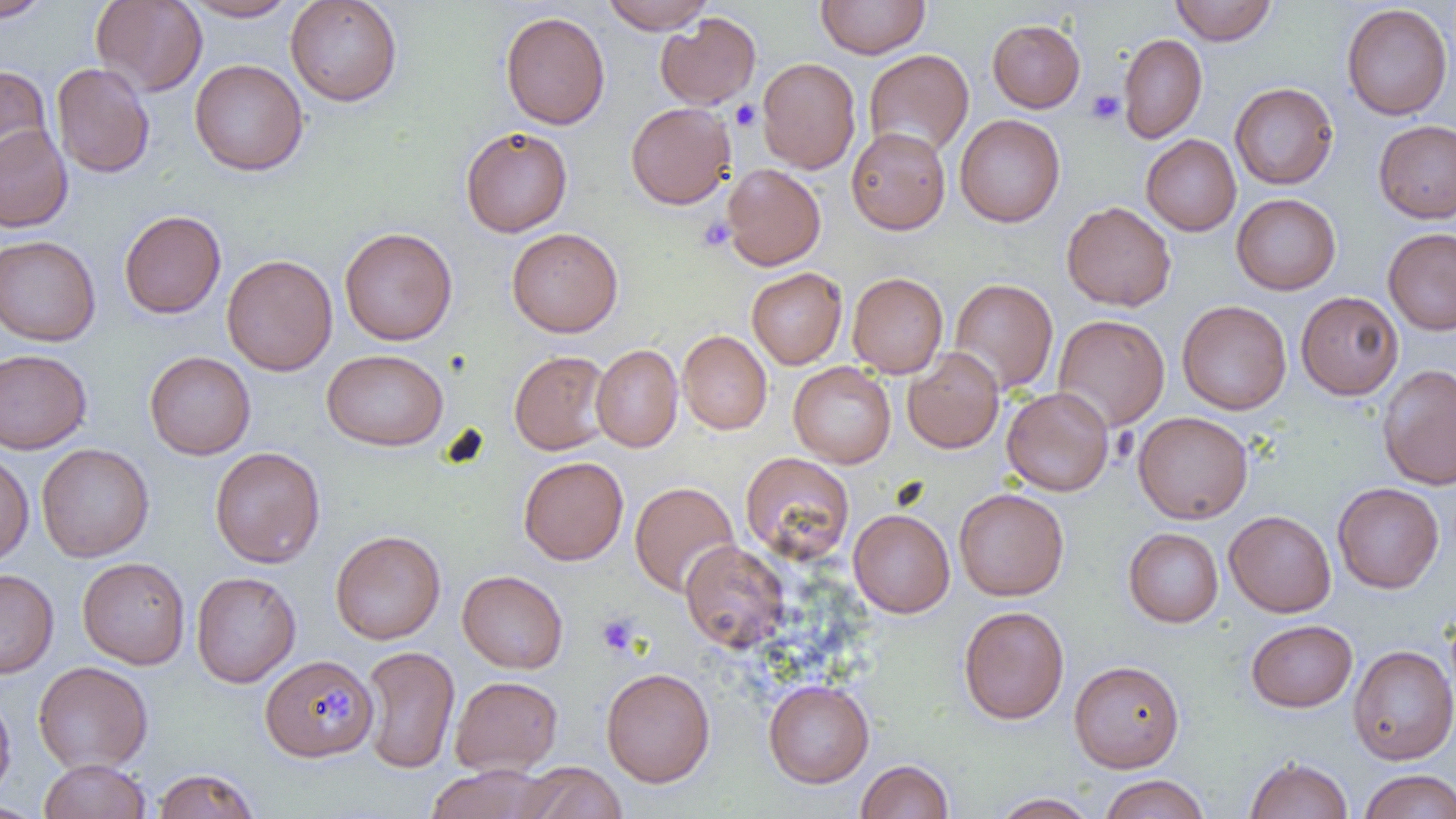 Approximate bounding boxes as named x1/y1/x2/y2 corners in pixels. Uninfected red blood cell locations: (x1=0, y1=0, x2=54, y2=22), (x1=182, y1=0, x2=302, y2=22), (x1=285, y1=0, x2=403, y2=106), (x1=599, y1=0, x2=716, y2=32), (x1=816, y1=0, x2=929, y2=59), (x1=1170, y1=0, x2=1276, y2=45), (x1=91, y1=1, x2=207, y2=96), (x1=1341, y1=3, x2=1453, y2=120), (x1=500, y1=11, x2=610, y2=130), (x1=655, y1=12, x2=761, y2=109), (x1=987, y1=19, x2=1085, y2=112), (x1=1118, y1=33, x2=1207, y2=143), (x1=863, y1=49, x2=974, y2=158), (x1=757, y1=57, x2=861, y2=174), (x1=189, y1=58, x2=309, y2=176), (x1=51, y1=63, x2=155, y2=178), (x1=0, y1=64, x2=54, y2=178), (x1=1229, y1=82, x2=1338, y2=189), (x1=626, y1=102, x2=736, y2=209), (x1=954, y1=114, x2=1065, y2=227), (x1=1373, y1=120, x2=1456, y2=223), (x1=0, y1=125, x2=73, y2=232), (x1=460, y1=126, x2=573, y2=237), (x1=846, y1=127, x2=951, y2=234), (x1=1141, y1=134, x2=1241, y2=236), (x1=722, y1=163, x2=826, y2=270), (x1=1231, y1=193, x2=1341, y2=294), (x1=1061, y1=201, x2=1176, y2=311), (x1=119, y1=210, x2=226, y2=319), (x1=339, y1=227, x2=457, y2=345), (x1=507, y1=227, x2=623, y2=337), (x1=1383, y1=227, x2=1456, y2=334), (x1=0, y1=235, x2=101, y2=346), (x1=222, y1=254, x2=338, y2=376), (x1=747, y1=268, x2=847, y2=369), (x1=847, y1=272, x2=948, y2=378), (x1=949, y1=278, x2=1058, y2=394), (x1=1296, y1=291, x2=1404, y2=399), (x1=1177, y1=300, x2=1292, y2=415), (x1=1053, y1=314, x2=1170, y2=431), (x1=678, y1=330, x2=772, y2=434), (x1=591, y1=344, x2=683, y2=452), (x1=0, y1=348, x2=92, y2=454), (x1=903, y1=348, x2=1004, y2=453), (x1=322, y1=349, x2=448, y2=451), (x1=509, y1=350, x2=612, y2=455), (x1=144, y1=351, x2=256, y2=459), (x1=788, y1=361, x2=896, y2=468), (x1=1377, y1=364, x2=1456, y2=489), (x1=1001, y1=386, x2=1114, y2=496), (x1=1133, y1=411, x2=1253, y2=523), (x1=36, y1=443, x2=154, y2=562), (x1=210, y1=446, x2=325, y2=568), (x1=0, y1=450, x2=34, y2=566), (x1=740, y1=452, x2=855, y2=564), (x1=518, y1=456, x2=628, y2=565), (x1=629, y1=481, x2=740, y2=597), (x1=1332, y1=482, x2=1444, y2=593), (x1=954, y1=488, x2=1069, y2=600), (x1=849, y1=509, x2=954, y2=618), (x1=1224, y1=510, x2=1336, y2=617), (x1=1124, y1=527, x2=1223, y2=627), (x1=331, y1=530, x2=446, y2=644), (x1=680, y1=541, x2=789, y2=652), (x1=77, y1=557, x2=190, y2=669), (x1=0, y1=569, x2=59, y2=679), (x1=458, y1=570, x2=568, y2=673), (x1=191, y1=571, x2=301, y2=687), (x1=958, y1=605, x2=1069, y2=724), (x1=1246, y1=619, x2=1357, y2=712), (x1=1348, y1=645, x2=1456, y2=764), (x1=360, y1=646, x2=460, y2=773), (x1=259, y1=654, x2=376, y2=761), (x1=1069, y1=660, x2=1184, y2=772), (x1=33, y1=661, x2=153, y2=773), (x1=601, y1=667, x2=715, y2=787), (x1=450, y1=675, x2=563, y2=774), (x1=763, y1=680, x2=874, y2=787), (x1=0, y1=688, x2=16, y2=805), (x1=1244, y1=756, x2=1353, y2=819), (x1=39, y1=758, x2=152, y2=819), (x1=855, y1=759, x2=954, y2=819), (x1=518, y1=762, x2=626, y2=819), (x1=424, y1=765, x2=558, y2=819), (x1=150, y1=768, x2=261, y2=819), (x1=1358, y1=769, x2=1456, y2=819), (x1=1099, y1=774, x2=1211, y2=819), (x1=991, y1=793, x2=1099, y2=818), (x1=0, y1=802, x2=45, y2=819). Platelet locations: (x1=1086, y1=90, x2=1124, y2=125), (x1=730, y1=100, x2=761, y2=131), (x1=697, y1=215, x2=735, y2=251), (x1=595, y1=612, x2=640, y2=657), (x1=320, y1=691, x2=355, y2=726). Slide-level diagnosis: negative for blood parasites. Single field of view. Optical microscopy. Thin blood film. 1000x magnification. Image is 1456×819 pixels.